Report the malaria status of this cell.
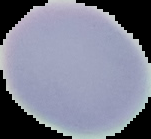

Uninfected.

Summary:
  - Image size: 151×139 pixels
  - Preparation: thin blood film
  - Image type: segmented cell region on a black background